Classify this cell by malaria status.
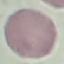
It is uninfected.

{
  "preparation": "thin blood film",
  "image_type": "cell patch, automatically extracted from a larger field of view and resized to 64 × 64 pixels",
  "stain": "Giemsa",
  "capture": "smartphone through the microscope eyepiece"
}